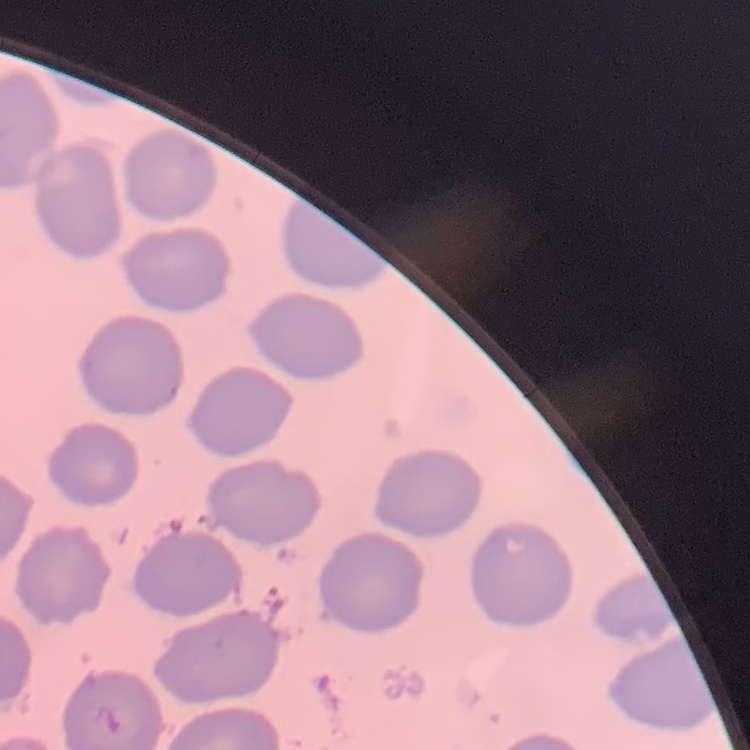

{
  "erythrocyte_morphology": "no rouleaux formation",
  "image_type": "one tile cut from a larger photomicrograph",
  "preparation": "thin peripheral smear",
  "stain": "Field's or Giemsa"
}